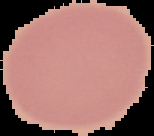
From a thin blood smear. Image is 154×136 pixels. The area outside the segmented cell region is set to black. Malaria status: uninfected.